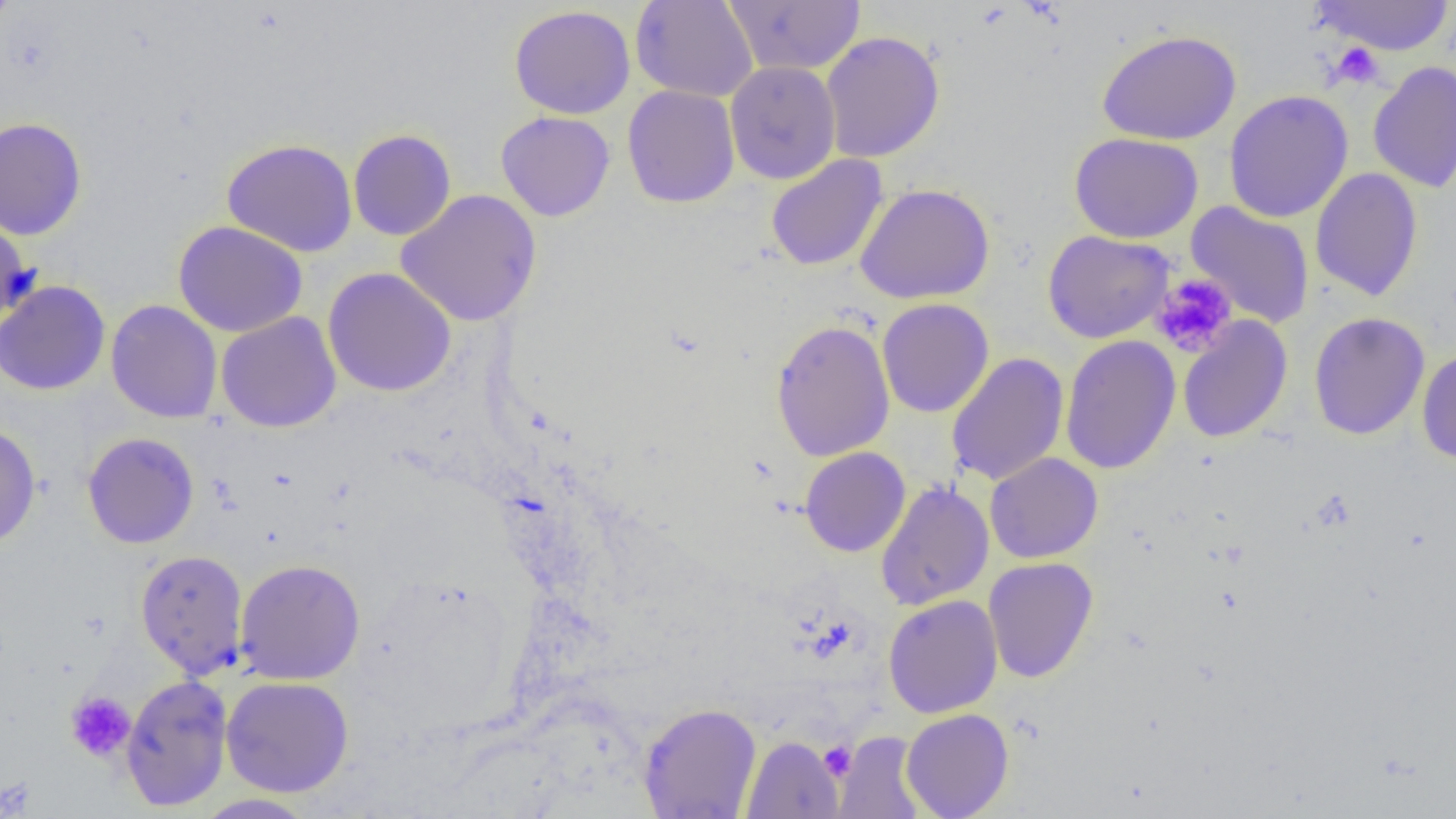

slide_level_diagnosis: negative for blood parasites
preparation: thin blood film
uninfected_red_blood_cell_locations: 'approximate bounding boxes as (x1, y1, x2, y2) in pixels: (0, 0, 17, 36), (630, 0, 759, 102), (725, 0, 866, 75), (1310, 0, 1456, 55), (509, 5, 636, 119), (1097, 29, 1242, 146), (820, 30, 945, 163), (724, 61, 841, 184), (1367, 61, 1456, 194), (622, 85, 740, 208), (1223, 89, 1355, 223), (496, 110, 615, 222), (0, 117, 87, 241), (348, 129, 456, 241), (1069, 132, 1203, 243), (220, 138, 357, 258), (766, 153, 888, 272), (1310, 168, 1424, 302), (855, 183, 995, 305), (395, 189, 542, 327), (1185, 201, 1315, 329), (0, 215, 35, 329), (173, 220, 308, 338), (1042, 230, 1175, 343), (323, 267, 457, 397), (0, 280, 111, 395), (1, 290, 223, 404), (877, 298, 994, 417), (105, 299, 222, 423), (216, 311, 342, 433), (1308, 312, 1430, 440), (1177, 316, 1292, 444), (770, 319, 895, 461), (1060, 335, 1181, 474), (1416, 348, 1456, 464), (945, 352, 1069, 487), (0, 423, 41, 550), (82, 432, 199, 549), (799, 446, 910, 557), (985, 452, 1103, 563), (875, 481, 995, 611), (135, 549, 249, 679), (983, 557, 1098, 684), (235, 558, 365, 685), (883, 594, 1003, 719), (119, 674, 233, 811), (221, 676, 354, 797), (638, 703, 762, 818), (901, 708, 1014, 819), (833, 730, 926, 819), (741, 736, 844, 818), (193, 793, 318, 818)'
magnification: 1000x
field_of_view: one of a larger specimen
modality: optical microscopy
image_size: 1456×819 pixels
platelet_locations: 'approximate bounding boxes as (x1, y1, x2, y2) in pixels: (1329, 41, 1385, 89), (1150, 273, 1239, 358), (65, 691, 136, 762), (819, 739, 857, 780)'